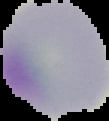
Summary:
  - Image size: 109×121 pixels
  - Malaria status: uninfected
  - Image type: segmented cell region on a black background
  - Preparation: thin blood film